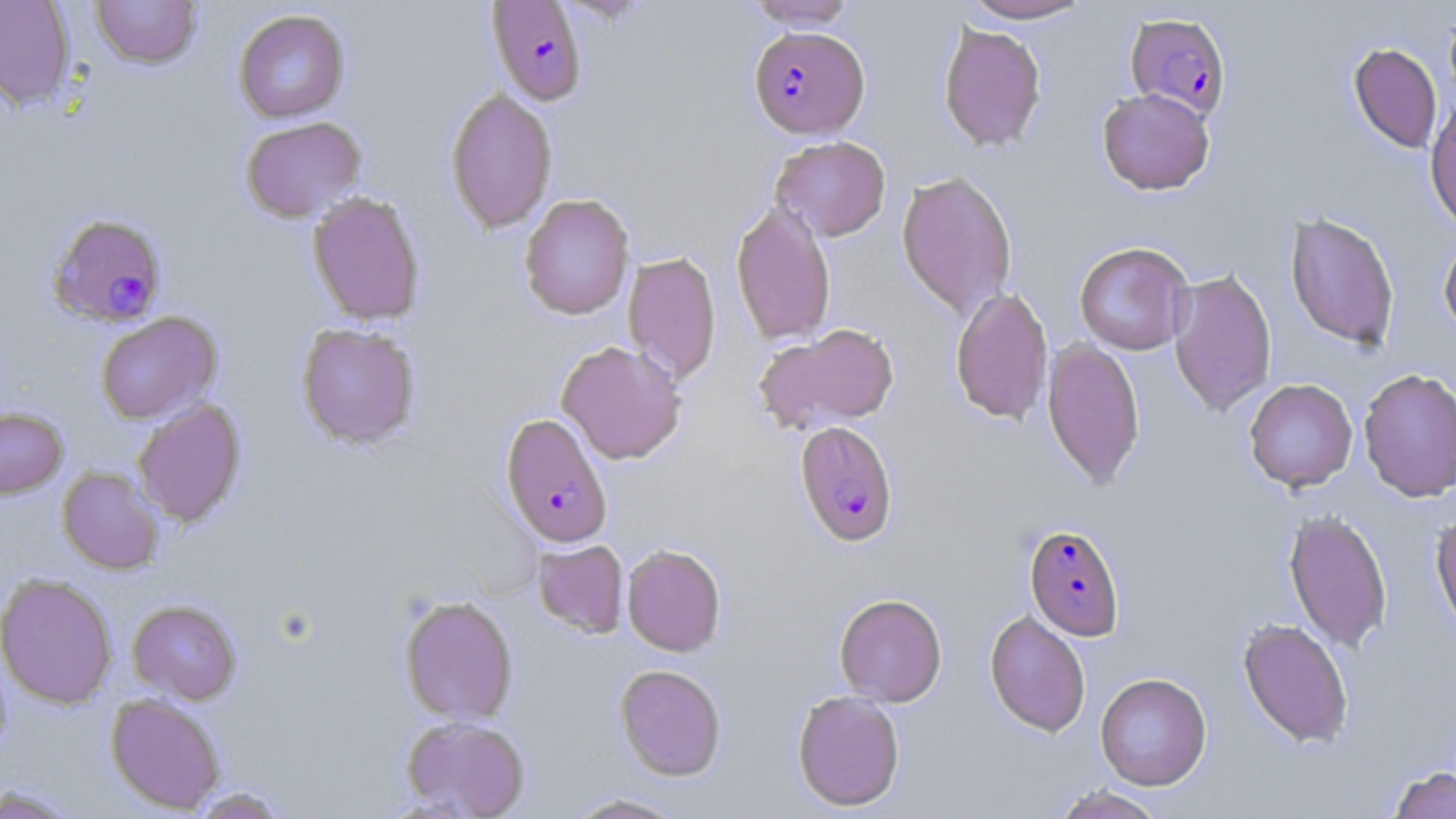
slide-level diagnosis = Plasmodium falciparum
magnification = 1000x
Plasmodium falciparum-infected red blood cell locations = approximate bounding boxes as named x1/y1/x2/y2 corners in pixels: (x1=488, y1=1, x2=588, y2=106), (x1=1125, y1=11, x2=1231, y2=121), (x1=749, y1=26, x2=869, y2=139), (x1=46, y1=212, x2=168, y2=328), (x1=500, y1=413, x2=613, y2=548), (x1=795, y1=421, x2=898, y2=547), (x1=1024, y1=524, x2=1124, y2=639)
field of view = single
image size = 1456×819 pixels
uninfected red blood cell locations = approximate bounding boxes as named x1/y1/x2/y2 corners in pixels: (x1=0, y1=0, x2=76, y2=111), (x1=90, y1=0, x2=202, y2=70), (x1=745, y1=0, x2=857, y2=29), (x1=959, y1=0, x2=1095, y2=23), (x1=233, y1=9, x2=350, y2=123), (x1=938, y1=22, x2=1047, y2=152), (x1=1348, y1=43, x2=1442, y2=154), (x1=445, y1=87, x2=558, y2=234), (x1=1097, y1=88, x2=1215, y2=195), (x1=1425, y1=96, x2=1456, y2=233), (x1=240, y1=117, x2=366, y2=223), (x1=771, y1=136, x2=891, y2=241), (x1=896, y1=170, x2=1018, y2=318), (x1=307, y1=192, x2=425, y2=326), (x1=519, y1=193, x2=635, y2=320), (x1=731, y1=200, x2=836, y2=346), (x1=1284, y1=212, x2=1400, y2=352), (x1=1438, y1=235, x2=1456, y2=340), (x1=1074, y1=241, x2=1194, y2=355), (x1=623, y1=251, x2=722, y2=385), (x1=1168, y1=268, x2=1277, y2=417), (x1=950, y1=287, x2=1053, y2=425), (x1=95, y1=312, x2=221, y2=424), (x1=296, y1=323, x2=420, y2=448), (x1=753, y1=323, x2=899, y2=434), (x1=1042, y1=338, x2=1145, y2=491), (x1=556, y1=339, x2=687, y2=465), (x1=1358, y1=367, x2=1456, y2=502), (x1=1244, y1=378, x2=1358, y2=492), (x1=132, y1=398, x2=246, y2=528), (x1=0, y1=406, x2=68, y2=499), (x1=57, y1=466, x2=164, y2=575), (x1=1283, y1=508, x2=1393, y2=653), (x1=1431, y1=511, x2=1456, y2=640), (x1=533, y1=540, x2=628, y2=638), (x1=622, y1=544, x2=726, y2=656), (x1=0, y1=572, x2=118, y2=709), (x1=834, y1=593, x2=947, y2=706), (x1=399, y1=595, x2=519, y2=725), (x1=128, y1=600, x2=241, y2=704), (x1=985, y1=610, x2=1091, y2=737), (x1=1237, y1=617, x2=1354, y2=748), (x1=615, y1=664, x2=727, y2=781), (x1=1095, y1=672, x2=1212, y2=790), (x1=791, y1=690, x2=905, y2=811), (x1=106, y1=693, x2=225, y2=814), (x1=401, y1=716, x2=531, y2=818), (x1=1387, y1=766, x2=1455, y2=818), (x1=0, y1=784, x2=81, y2=818), (x1=1051, y1=785, x2=1168, y2=818), (x1=188, y1=787, x2=290, y2=817), (x1=564, y1=793, x2=690, y2=818)
preparation = thin blood film
stain = May-Grünwald-Giemsa
modality = optical microscopy